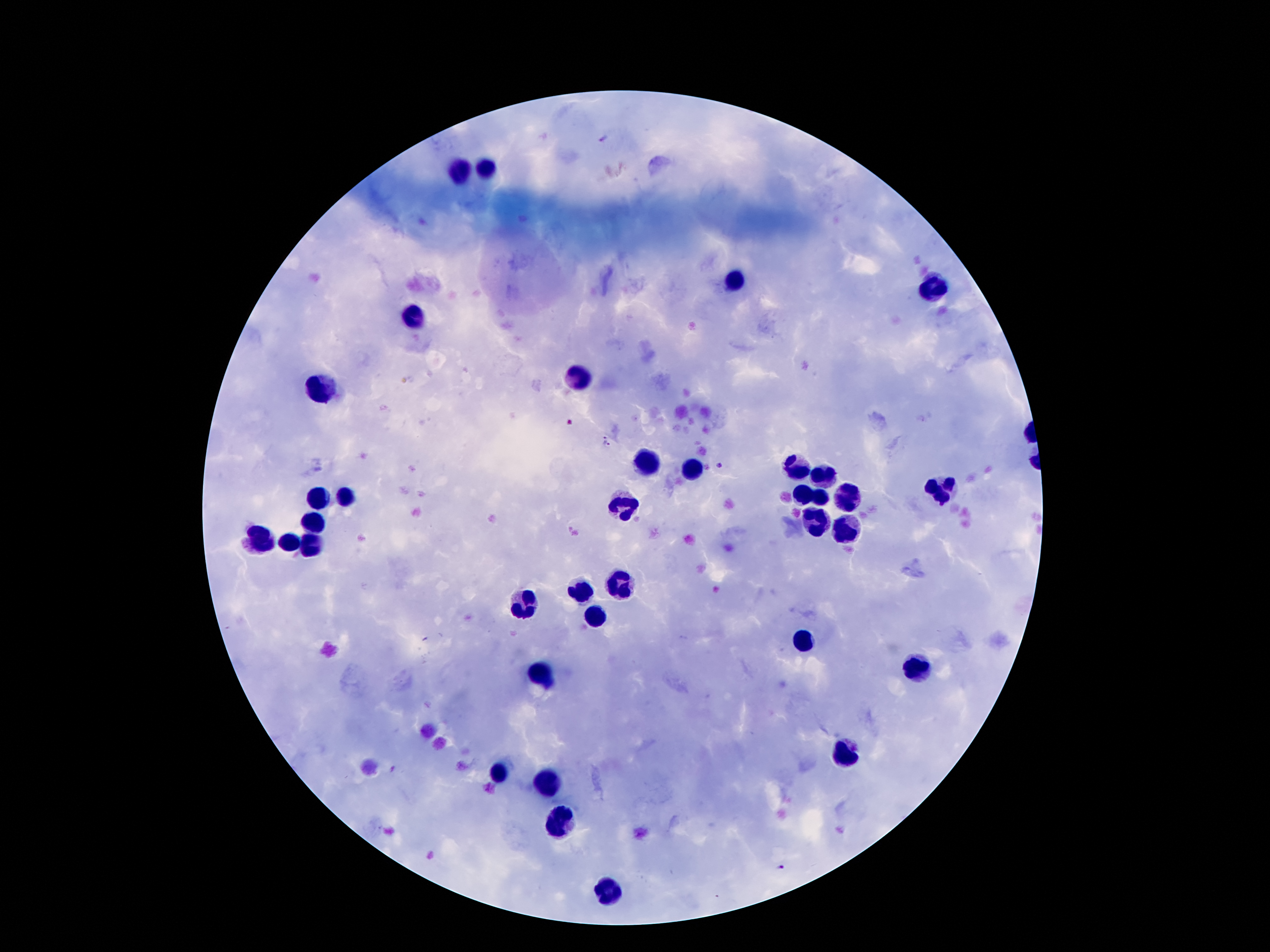 Approximate centers as {x, y} in pixels. Leukocyte locations: {484, 168}, {459, 170}, {736, 285}, {936, 291}, {411, 314}, {575, 379}, {316, 386}, {650, 465}, {797, 468}, {690, 470}, {822, 476}, {943, 490}, {801, 493}, {846, 495}, {348, 497}, {820, 497}, {319, 499}, {623, 504}, {316, 522}, {816, 524}, {843, 527}, {258, 541}, {291, 544}, {310, 545}, {618, 584}, {581, 592}, {525, 605}, {594, 616}, {805, 640}, {917, 669}, {540, 672}, {843, 754}, {502, 772}, {545, 780}, {558, 820}, {606, 891}. Plasmodium parasite locations: {602, 138}, {606, 441}, {718, 465}, {784, 870}. Patient malaria status: positive for Plasmodium falciparum. Giemsa-stained preparation. 100x magnification. Smartphone photograph taken through the microscope eyepiece. Thick blood film. Image is 1270×952 pixels. Single field of view.